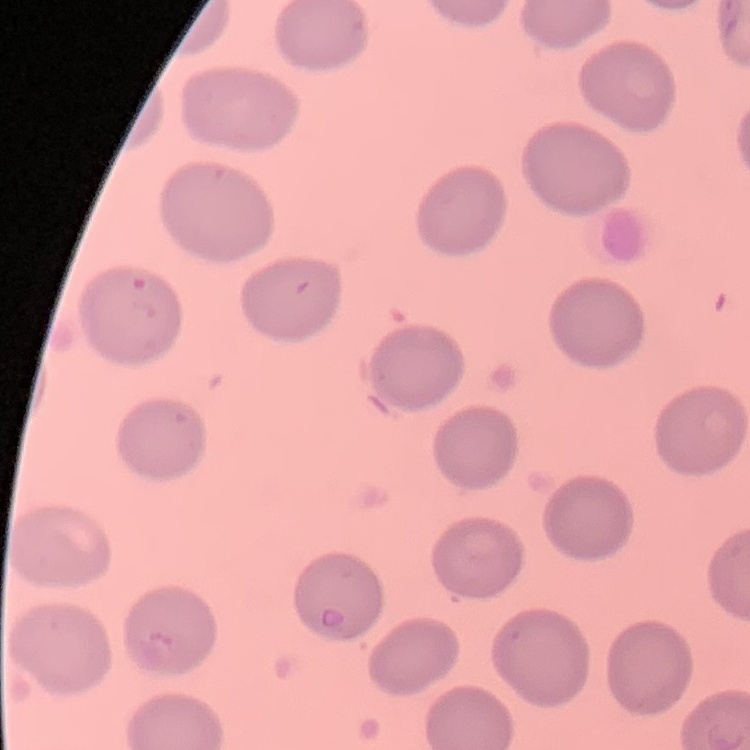
Summary:
  - Erythrocyte morphology: no rouleaux formation
  - Preparation: thin blood smear
  - Image type: square crop of a larger photomicrograph
  - Stain: Field's or Giemsa